Report the malaria status of this cell.
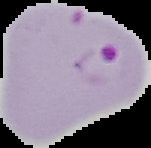

Parasitized.

{
  "preparation": "thin blood film",
  "image_size": "151×148 pixels",
  "image_type": "segmented cell region on a black background"
}